Identify the cell.
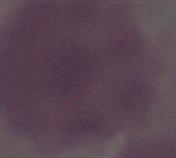
An erythrocyte.

Photomicrograph. Captured at 1000x magnification.